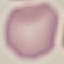
{
  "result": "no malaria parasites detected",
  "image_type": "cell patch, automatically extracted from a larger field of view and resized to 64 × 64 pixels",
  "capture": "smartphone through the microscope eyepiece",
  "stain": "Giemsa",
  "preparation": "thin blood film"
}